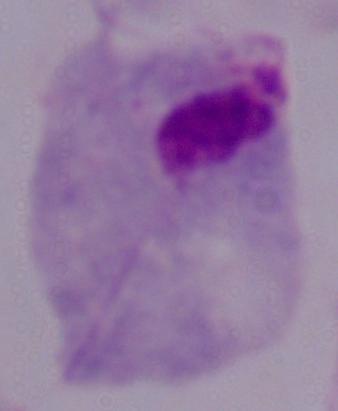
Micrograph. A trichomonad is shown. Captured at 1000x magnification.